Identify the parasite.
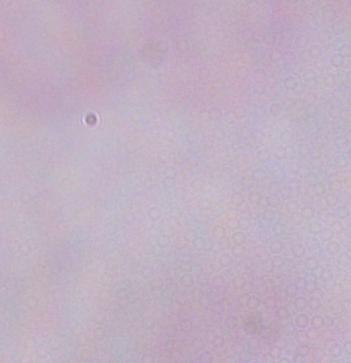
A trypanosome.

1000x magnification. Photomicrograph.